Classify this cell by malaria status.
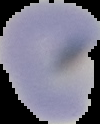
It is uninfected.

Summary:
  - Preparation: thin blood film
  - Image size: 100×124 pixels
  - Image type: segmented cell region on a black background